Assess this cell for malaria.
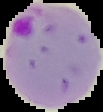
It is parasitized.

Image is 103×112 pixels. Cell region segmented out of the field of view; the surrounding area is masked to black. From a thin blood smear.